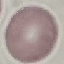
Summary:
  - Result: no malaria parasites seen
  - Image type: automatically extracted cell patch, resized to 64 × 64 pixels
  - Preparation: thin blood smear
  - Capture: smartphone camera at the microscope eyepiece
  - Stain: Giemsa